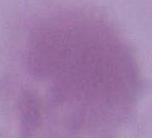
Summary:
  - Identification: red blood cell
  - Magnification: 1000x
  - Modality: micrograph